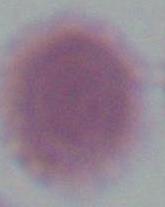

1000x magnification. An erythrocyte is shown. Micrograph.